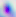 Micrograph. Toxoplasma gondii is seen. 400x magnification.